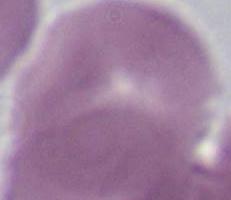
modality = photomicrograph
identification = erythrocyte
magnification = 1000x